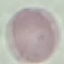

result = no malaria parasites detected
stain = Giemsa
preparation = thin blood film
capture = smartphone through the microscope eyepiece
image type = automatically extracted cell patch, resized to 64 × 64 pixels